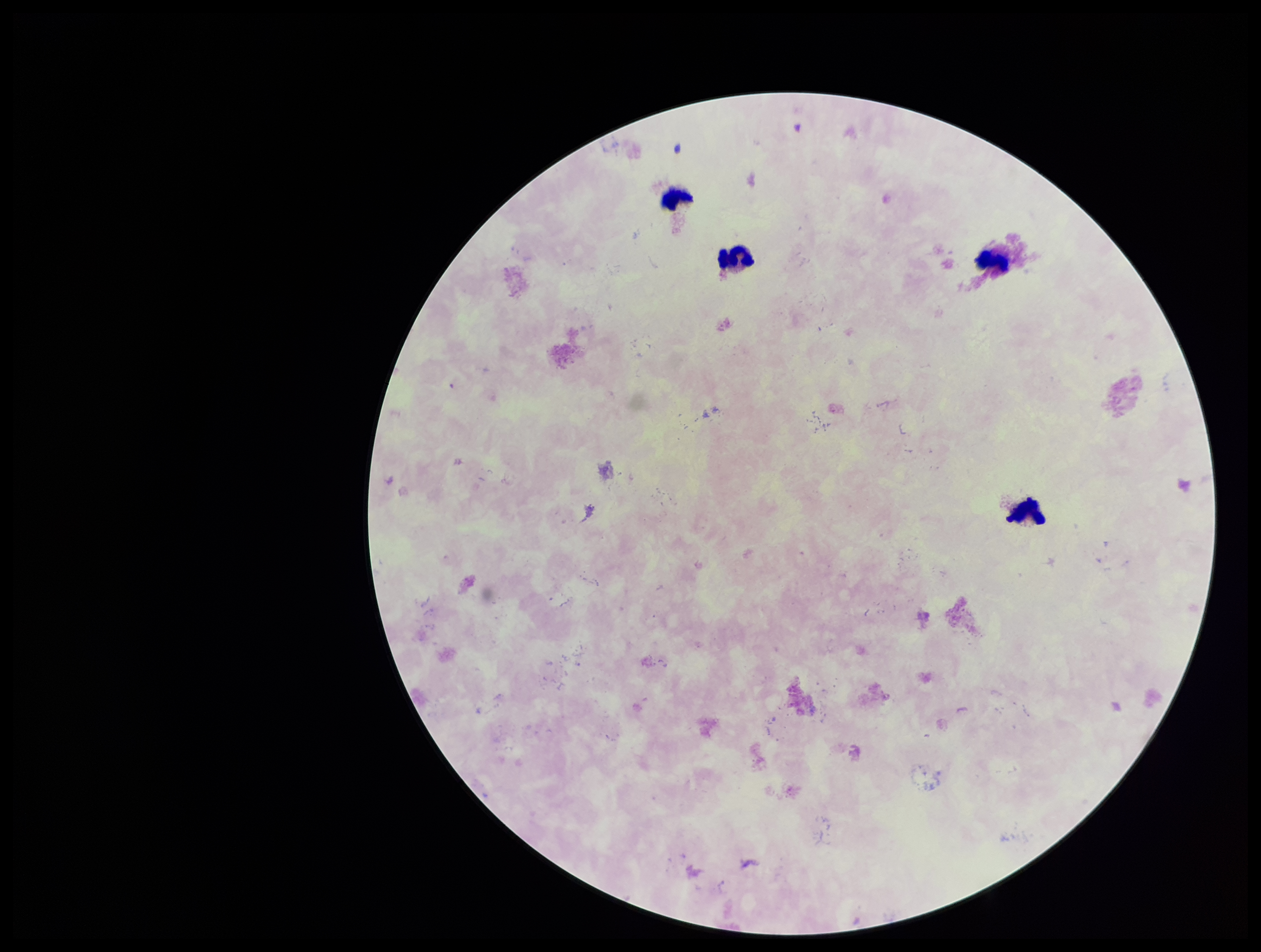
capture = smartphone photograph through the microscope eyepiece
parasite count = 0
leukocyte count = 4
stain = Giemsa
Plasmodium parasites = none seen
preparation = thick blood smear
field of view = single
patient malaria status = negative
image size = 1261×952 pixels